Report the malaria status of this cell.
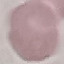
It is uninfected.

Automatically extracted cell patch, resized to 64 × 64 pixels. Photographed with a smartphone camera at the microscope eyepiece. Giemsa-stained preparation. Thin blood smear.